Describe the morphology of the red blood cells.
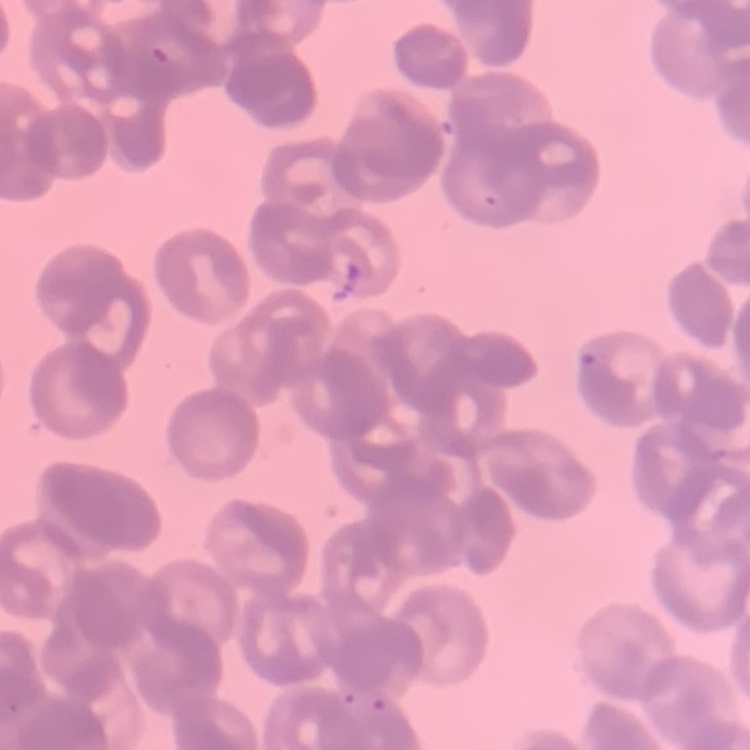

Rouleaux formation.

Summary:
  - Image type: one tile cut from a larger photomicrograph
  - Stain: Field's or Giemsa
  - Preparation: thin blood film